Assess this cell for malaria.
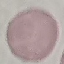
It is uninfected.

Summary:
  - Image type: automatically extracted cell patch, resized to 64 × 64 pixels
  - Capture: smartphone through the microscope eyepiece
  - Stain: Giemsa
  - Preparation: thin blood smear